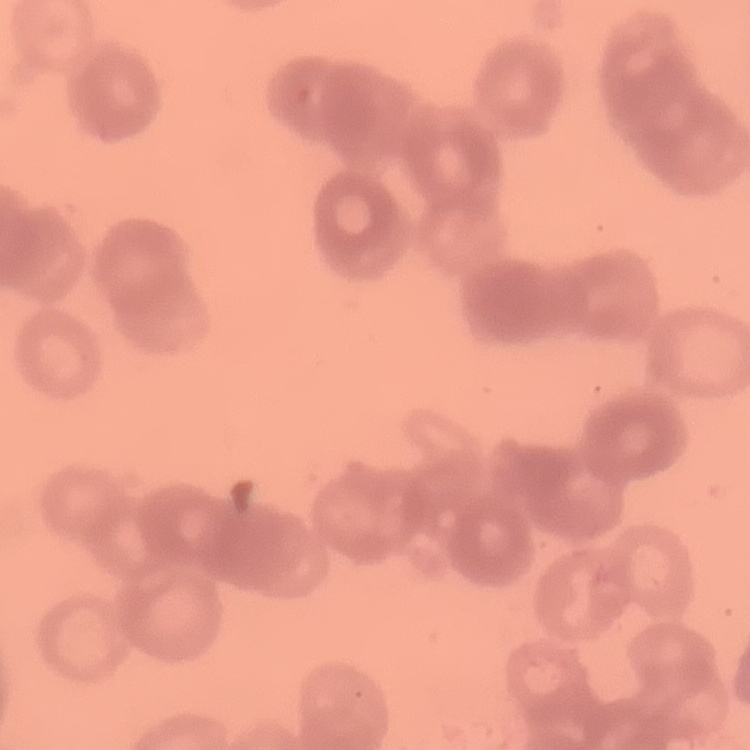

The erythrocytes exhibit rouleaux formation. Thin blood smear. One tile cut from a larger photomicrograph. Stained with either Field's or Giemsa.